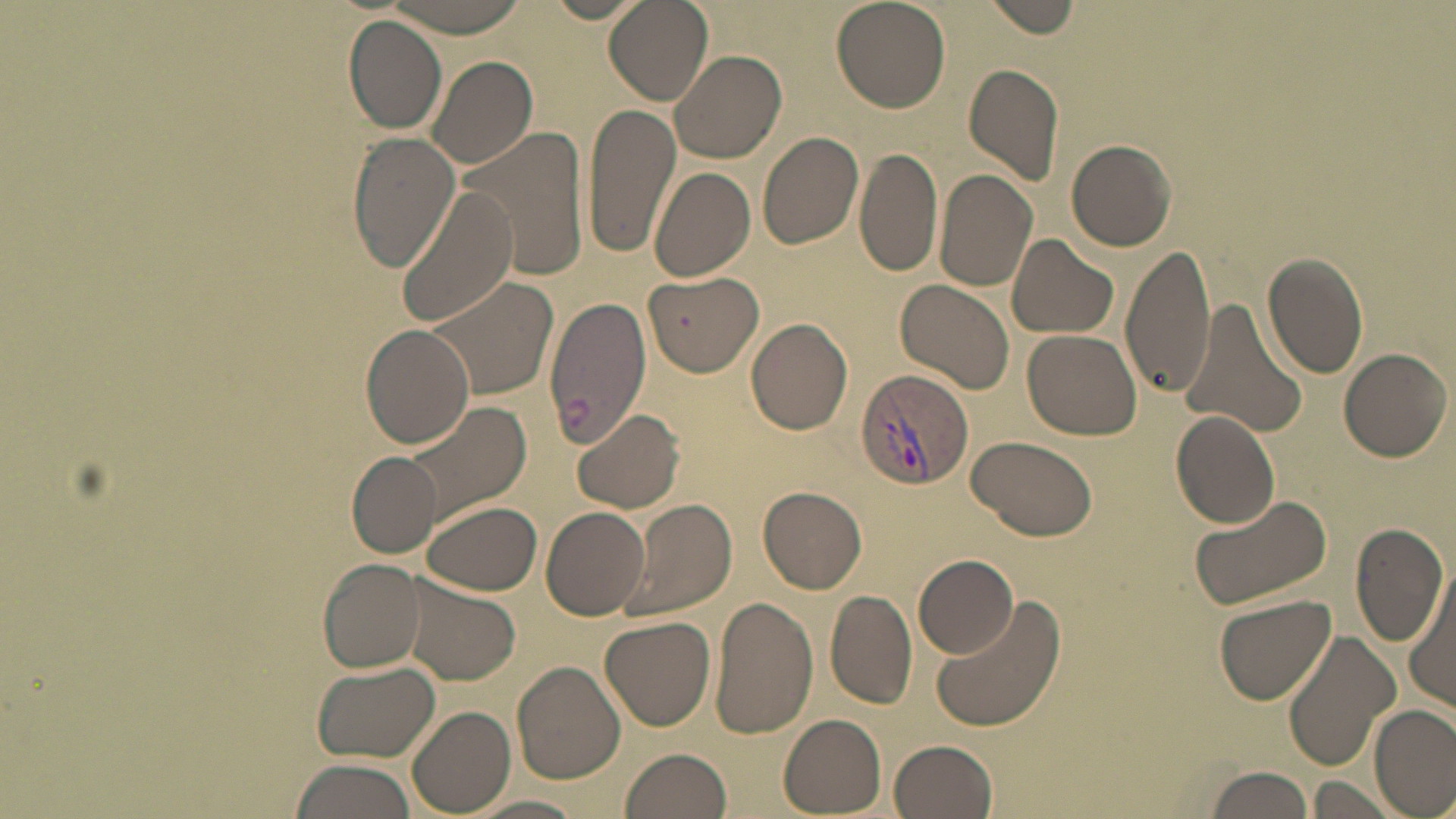
{
  "slide_level_diagnosis": "Plasmodium vivax",
  "field_of_view": "one of a larger specimen",
  "uninfected_red_blood_cell_locations": "approximate bounding boxes as named x1/y1/x2/y2 corners in pixels: (x1=603, y1=0, x2=714, y2=106), (x1=829, y1=0, x2=951, y2=113), (x1=982, y1=0, x2=1083, y2=38), (x1=382, y1=1, x2=535, y2=35), (x1=343, y1=16, x2=447, y2=133), (x1=670, y1=49, x2=787, y2=164), (x1=426, y1=55, x2=540, y2=170), (x1=963, y1=62, x2=1064, y2=187), (x1=583, y1=101, x2=680, y2=261), (x1=461, y1=125, x2=592, y2=286), (x1=756, y1=131, x2=864, y2=251), (x1=347, y1=133, x2=459, y2=271), (x1=1066, y1=138, x2=1178, y2=252), (x1=855, y1=147, x2=941, y2=281), (x1=648, y1=164, x2=755, y2=283), (x1=934, y1=170, x2=1039, y2=292), (x1=397, y1=186, x2=520, y2=328), (x1=1006, y1=234, x2=1118, y2=339), (x1=1120, y1=243, x2=1216, y2=399), (x1=1261, y1=251, x2=1370, y2=378), (x1=645, y1=272, x2=763, y2=375), (x1=421, y1=274, x2=559, y2=405), (x1=895, y1=278, x2=1016, y2=397), (x1=545, y1=295, x2=649, y2=448), (x1=1177, y1=298, x2=1308, y2=440), (x1=745, y1=317, x2=854, y2=435), (x1=361, y1=325, x2=475, y2=448), (x1=1023, y1=328, x2=1142, y2=440), (x1=1337, y1=347, x2=1450, y2=461), (x1=397, y1=399, x2=530, y2=530), (x1=571, y1=407, x2=686, y2=514), (x1=1170, y1=411, x2=1279, y2=529), (x1=964, y1=435, x2=1097, y2=542), (x1=349, y1=455, x2=440, y2=556), (x1=759, y1=486, x2=867, y2=593), (x1=1188, y1=495, x2=1333, y2=613), (x1=622, y1=499, x2=736, y2=624), (x1=421, y1=501, x2=542, y2=595), (x1=540, y1=506, x2=649, y2=620), (x1=1349, y1=521, x2=1449, y2=647), (x1=915, y1=552, x2=1021, y2=658), (x1=319, y1=559, x2=425, y2=673), (x1=1402, y1=567, x2=1455, y2=714), (x1=408, y1=576, x2=523, y2=688), (x1=825, y1=589, x2=918, y2=709), (x1=1212, y1=594, x2=1336, y2=705), (x1=932, y1=595, x2=1066, y2=733), (x1=708, y1=596, x2=817, y2=737), (x1=600, y1=616, x2=716, y2=731), (x1=1283, y1=629, x2=1398, y2=771), (x1=513, y1=662, x2=626, y2=784), (x1=312, y1=663, x2=441, y2=761), (x1=408, y1=706, x2=515, y2=814), (x1=1370, y1=706, x2=1455, y2=816), (x1=777, y1=714, x2=887, y2=816), (x1=889, y1=739, x2=999, y2=819), (x1=620, y1=747, x2=734, y2=818), (x1=290, y1=759, x2=419, y2=819), (x1=1199, y1=764, x2=1314, y2=819), (x1=1306, y1=777, x2=1402, y2=816), (x1=463, y1=797, x2=589, y2=819)",
  "modality": "light microscopy",
  "image_size": "1456×819 pixels",
  "plasmodium_vivax_infected_red_blood_cell_locations": "approximate bounding boxes as named x1/y1/x2/y2 corners in pixels: (x1=854, y1=368, x2=974, y2=492)",
  "preparation": "thin blood film",
  "stain": "May-Grünwald-Giemsa",
  "magnification": "1000x"
}